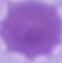

A red blood cell is shown. Captured at 1000x magnification. Photomicrograph.